Comment on the morphology of the erythrocytes.
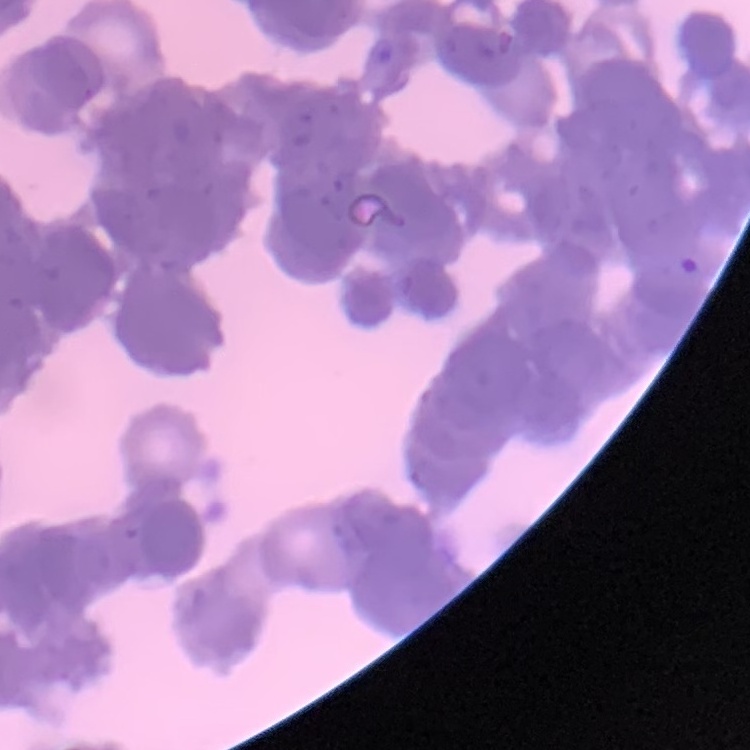

They show rouleaux formation.

Square crop of a larger photomicrograph. Stained with either Field's or Giemsa. Thin blood smear.